Classify this cell by malaria status.
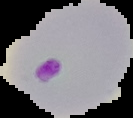
It is parasitized.

image_type: segmented cell region with the area outside set to black
image_size: 133×118 pixels
preparation: thin blood film